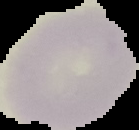

Summary:
  - Image type: cell region segmented out of the field of view; surrounding area masked to black
  - Preparation: thin blood film
  - Image size: 139×130 pixels
  - Result: no malaria parasites seen